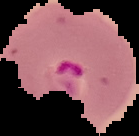
Summary:
  - Preparation: thin blood film
  - Malaria status: parasitized
  - Image type: segmented cell region with the area outside set to black
  - Image size: 139×136 pixels